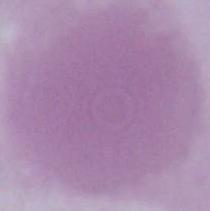

{
  "modality": "photomicrograph",
  "identification": "erythrocyte",
  "magnification": "1000x"
}